State which parasite is depicted.
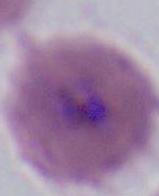

This is Plasmodium.

Captured at either 400x or 1000x magnification. Photomicrograph.